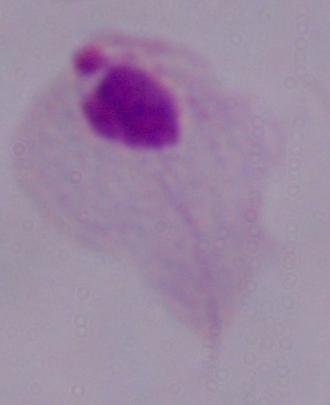 Photomicrograph. 1000x magnification. A trichomonad is shown.